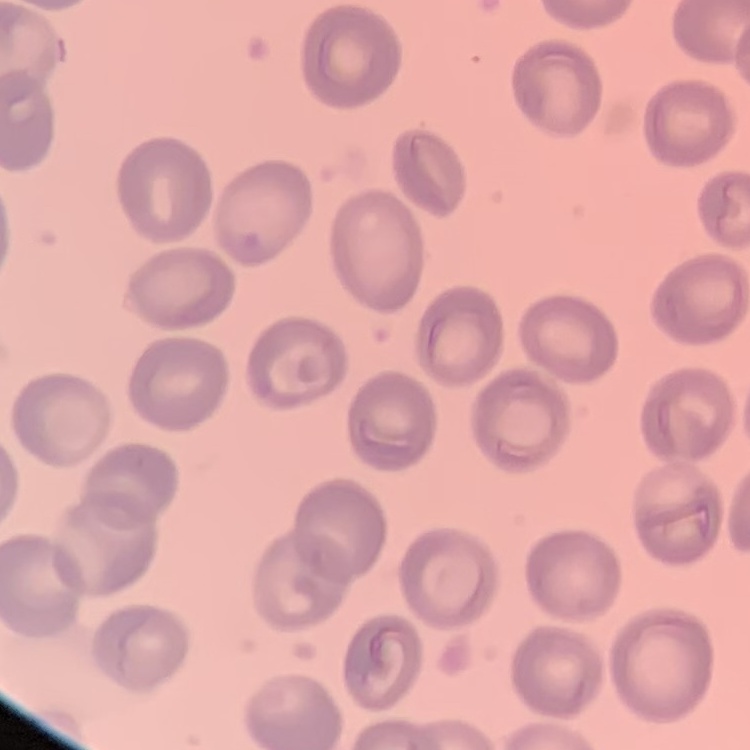

The erythrocytes show no rouleaux formation. Field's or Giemsa stain. Square crop of a larger photomicrograph. Thin blood film.